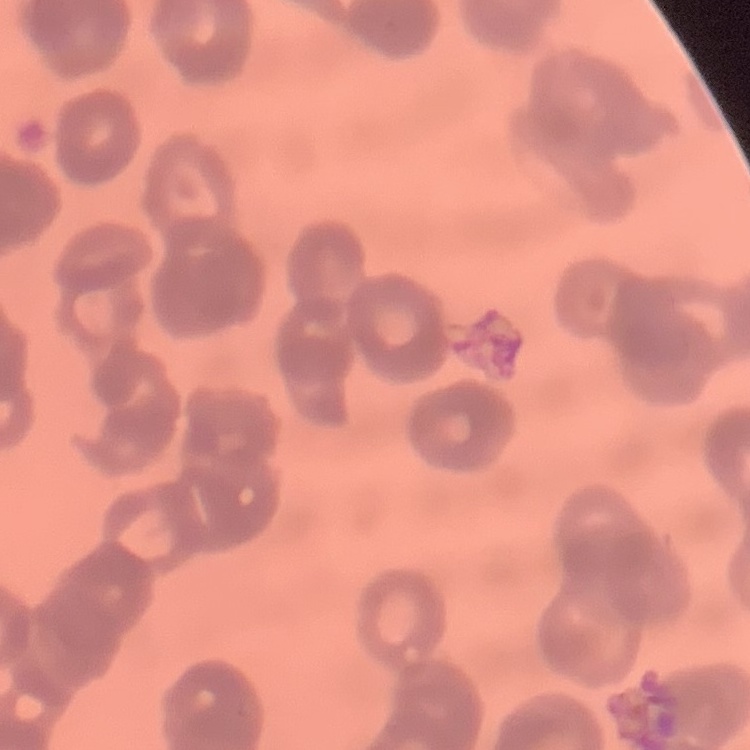

erythrocyte morphology = rouleaux formation
stain = Field's or Giemsa
image type = one tile cut from a larger photomicrograph
preparation = thin blood film